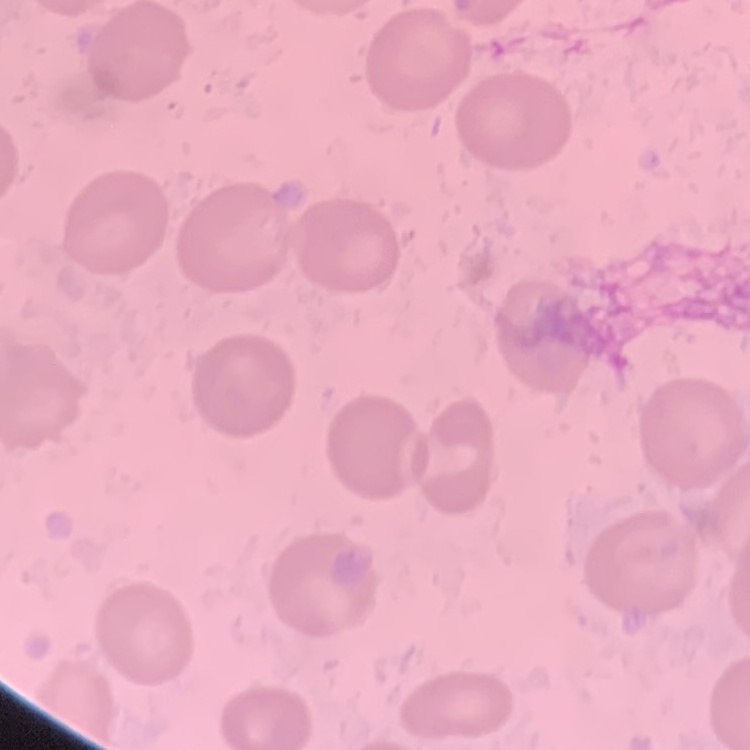 The erythrocytes exhibit no rouleaux formation. Field's or Giemsa stain. Square crop of a larger photomicrograph. Thin peripheral smear.